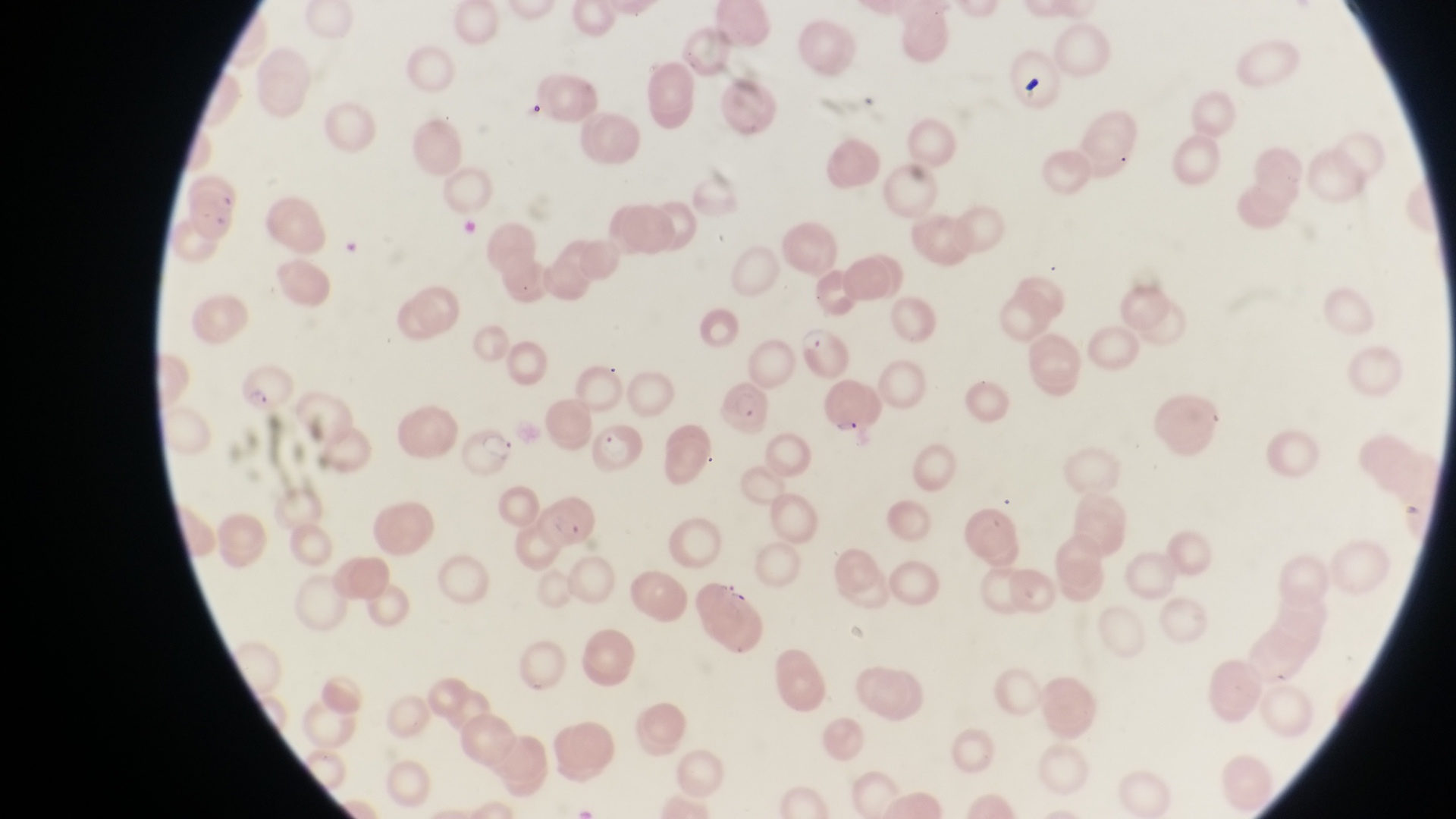
Approximate bounding boxes as (left, top, right, bottom) in pixels.
Summary:
  - Artifact (platelet-like body, stain precipitate, or debris) locations: (1020, 76, 1044, 103)
  - Parasitised red blood cell locations: (798, 325, 851, 380), (240, 362, 298, 417), (716, 380, 774, 439), (589, 420, 644, 479), (460, 428, 518, 480), (541, 494, 596, 550)
  - Image size: 1456×819 pixels
  - Capture: smartphone photograph through the eyepiece of an Olympus CX-23 microscope
  - Field of view: single
  - Preparation: thin blood smear
  - Magnification: 1000x
  - Country: Uganda